Describe the morphology of the red blood cells.
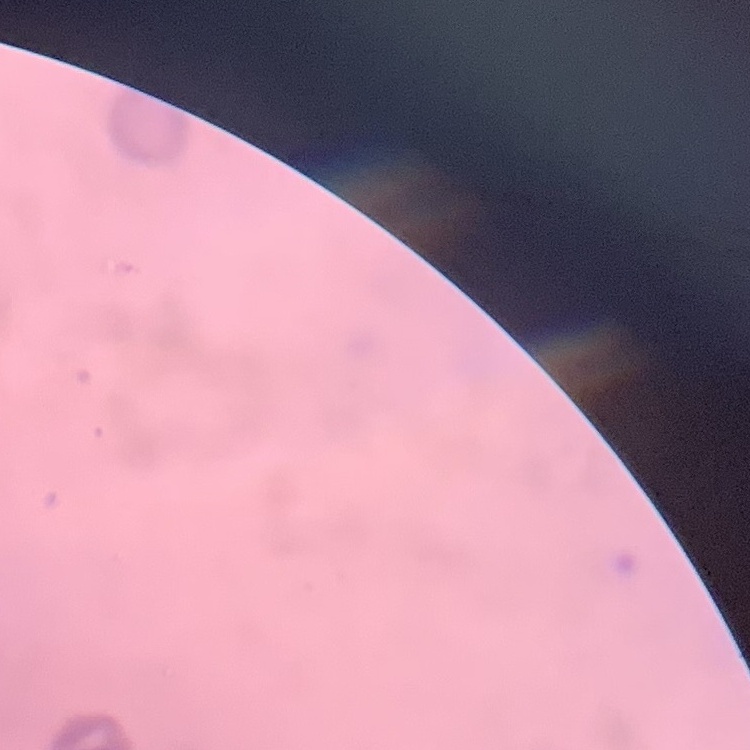

Rouleaux formation.

One tile cut from a larger photomicrograph. Thin blood film. Stained with either Field's or Giemsa.